Locate and identify every blood parasite.
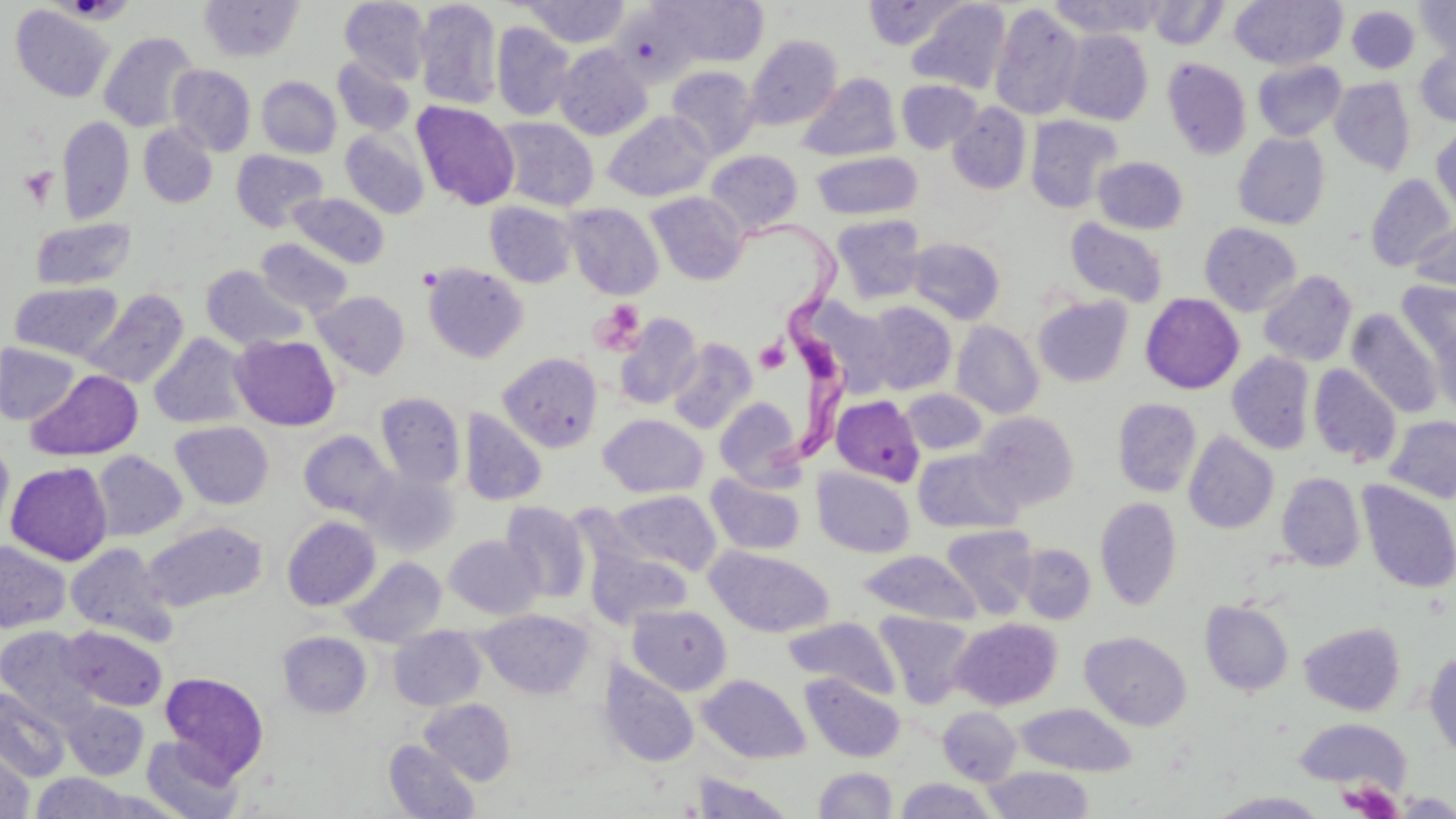
Approximate bounding boxes as (x1,y1)-(x2,y2) corner pairs in pixels.
Trypanosoma brucei: (744,212)-(859,477).
No Plasmodium falciparum, Plasmodium ovale, Plasmodium malariae, Plasmodium vivax, or Babesia divergens observed.

Platelet locations: (19,166)-(57,208), (590,300)-(646,355), (754,339)-(790,373), (1341,781)-(1401,818). Uninfected red blood cell locations: (199,0)-(303,62), (340,0)-(431,85), (414,0)-(502,110), (653,0)-(769,67), (863,0)-(967,50), (1046,0)-(1167,39), (1231,0)-(1347,70), (1415,0)-(1456,62), (520,1)-(632,47), (907,1)-(1011,94), (1147,1)-(1230,50), (990,2)-(1085,120), (10,5)-(115,102), (612,5)-(702,88), (1346,5)-(1420,73), (491,21)-(575,121), (1059,29)-(1153,125), (98,31)-(201,132), (744,34)-(843,130), (554,45)-(652,140), (1415,46)-(1456,125), (332,56)-(415,136), (1163,57)-(1252,160), (1253,59)-(1347,141), (167,64)-(256,156), (666,66)-(761,159), (797,73)-(901,161), (257,76)-(341,158), (1329,77)-(1416,175), (896,79)-(982,153), (412,101)-(520,210), (948,103)-(1031,194), (603,110)-(716,202), (56,115)-(134,223), (1026,115)-(1123,213), (493,117)-(599,211), (138,124)-(218,208), (1431,124)-(1456,222), (340,129)-(430,219), (1233,132)-(1331,229), (231,150)-(328,231), (706,150)-(803,234), (812,151)-(922,220), (1093,156)-(1188,234), (1365,173)-(1455,272), (646,191)-(749,285), (287,192)-(390,268), (485,201)-(578,288), (564,203)-(664,300), (831,214)-(927,304), (30,218)-(136,290), (1064,218)-(1169,308), (1410,220)-(1456,296), (1199,222)-(1302,316), (907,237)-(1005,324), (256,238)-(353,317), (421,262)-(529,363), (201,265)-(309,350), (1258,270)-(1357,366), (1397,280)-(1456,361), (9,281)-(123,361), (79,288)-(190,389), (312,290)-(410,379), (1140,293)-(1244,394), (1033,295)-(1132,386), (807,298)-(896,398), (863,301)-(957,394), (1346,309)-(1443,419), (614,313)-(703,410), (951,320)-(1044,419), (1430,322)-(1456,416), (149,333)-(250,429), (230,334)-(340,430), (667,337)-(757,434), (0,343)-(80,425), (1227,351)-(1315,454), (498,352)-(603,452), (1309,364)-(1402,467), (28,369)-(143,461), (899,389)-(987,455), (375,392)-(466,488), (831,395)-(924,485), (714,396)-(804,487), (1112,398)-(1202,497), (460,408)-(547,506), (974,411)-(1079,510), (598,414)-(708,498), (1385,415)-(1456,504), (171,421)-(274,509), (299,430)-(396,521), (1183,431)-(1279,534), (0,438)-(14,535), (913,449)-(1022,534), (92,450)-(187,541), (5,461)-(113,565), (362,468)-(460,558), (812,468)-(915,558), (705,472)-(807,556), (1276,472)-(1365,572), (1356,480)-(1456,593), (613,490)-(721,575), (1095,496)-(1183,611), (500,501)-(591,603), (283,516)-(380,610), (143,521)-(266,611), (941,524)-(1039,618), (444,534)-(543,619), (0,540)-(70,633), (66,542)-(179,646), (1017,543)-(1096,624), (586,545)-(693,630), (707,546)-(834,637), (857,550)-(983,626), (341,556)-(447,648), (1200,600)-(1294,696), (627,604)-(732,695), (477,609)-(594,699), (875,611)-(975,707), (784,617)-(899,698), (952,618)-(1062,710), (1299,621)-(1405,715), (0,626)-(99,723), (61,626)-(167,711), (389,626)-(487,710), (277,631)-(372,718), (1080,631)-(1192,731), (1425,649)-(1456,758), (600,660)-(699,767), (159,672)-(269,779), (802,673)-(905,763), (698,674)-(810,763), (0,688)-(71,782), (420,698)-(516,784), (60,700)-(149,780), (1014,703)-(1138,776), (937,706)-(1022,785), (1293,718)-(1411,792), (142,734)-(245,819), (384,739)-(480,819), (0,746)-(34,819), (982,765)-(1095,818), (813,766)-(899,817), (27,773)-(144,818), (691,773)-(795,818), (894,777)-(1000,819), (1208,791)-(1331,818). Slide-level diagnosis: Trypanosoma brucei. Light microscopy. Thin blood smear. Captured at 1000x magnification. Image is 1456×819 pixels. Single field of view. May-Grünwald-Giemsa stain.